Classify this cell by malaria status.
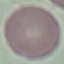

Uninfected.

Thin blood film. Giemsa stain. Photographed with a smartphone camera at the microscope eyepiece. Automatically extracted cell patch, resized to 64 × 64 pixels.